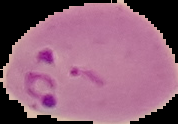

Summary:
  - Preparation: thin blood film
  - Image type: segmented cell region on a black background
  - Image size: 178×124 pixels
  - Malaria status: parasitized